Comment on the morphology of the red blood cells.
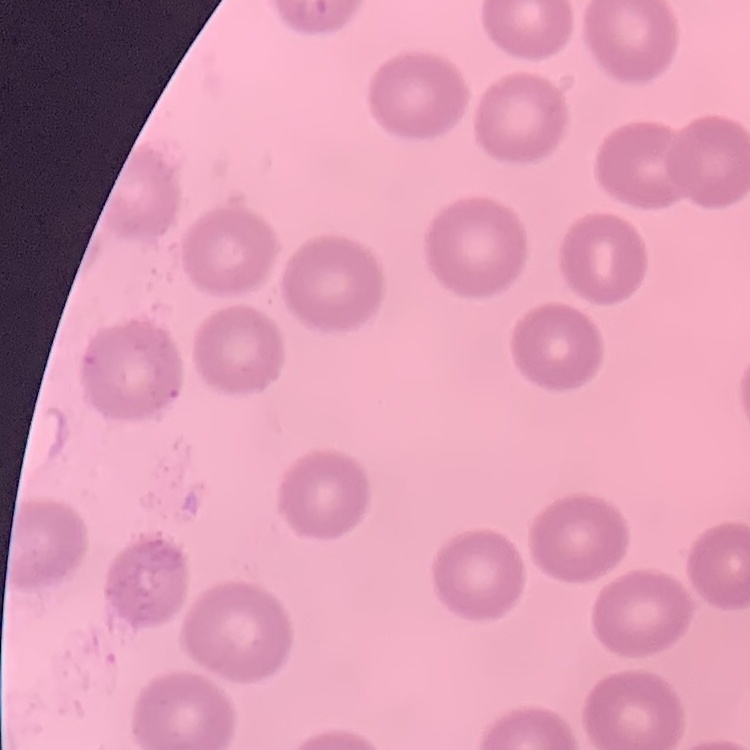

No rouleaux formation.

preparation: thin blood smear
image_type: square crop of a larger photomicrograph
stain: Field's or Giemsa